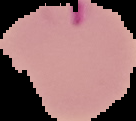

{
  "image_size": "136×121 pixels",
  "preparation": "thin blood smear",
  "result": "Plasmodium parasites identified",
  "image_type": "segmented cell region with the area outside set to black"
}